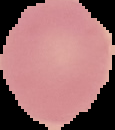
Summary:
  - Result: no malaria parasites seen
  - Image size: 115×130 pixels
  - Preparation: thin blood smear
  - Image type: segmented cell region on a black background